Assess this cell for malaria.
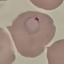
Parasitized.

stain = Giemsa
preparation = thin smear
capture = smartphone through the microscope eyepiece
image type = cell patch, automatically extracted from a larger field of view and resized to 64 × 64 pixels